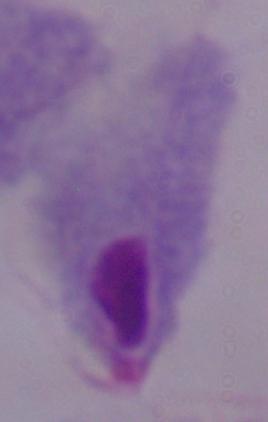
Summary:
  - Magnification: 1000x
  - Identification: trichomonad
  - Modality: micrograph